Draw a bounding box around every trophozoite.
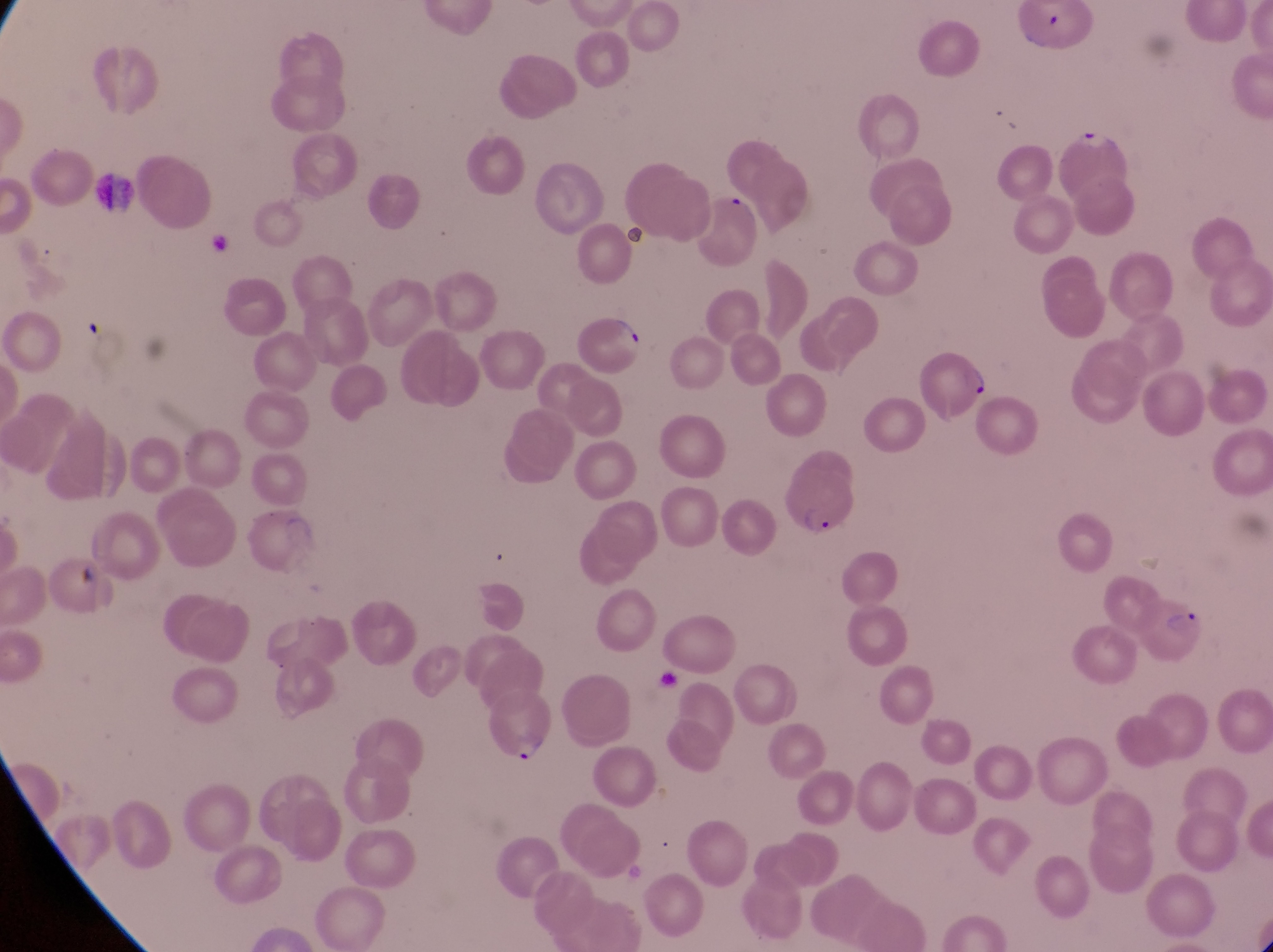
Approximate bounding boxes as (left, top, right, bottom) in pixels.
Trophozoites: (1074, 122, 1114, 159).

Summary:
  - Leukocyte locations: (87, 167, 137, 212)
  - Parasitised red blood cell locations: (574, 310, 651, 387), (914, 352, 989, 419), (781, 462, 866, 544), (1134, 591, 1214, 671), (475, 689, 557, 771)
  - Field of view: single
  - Country: Uganda
  - Capture: smartphone photograph through the eyepiece of an Olympus CX-23 microscope
  - Magnification: 1000x
  - Preparation: thin blood smear
  - Image size: 1273×952 pixels